Look for Plasmodium parasites.
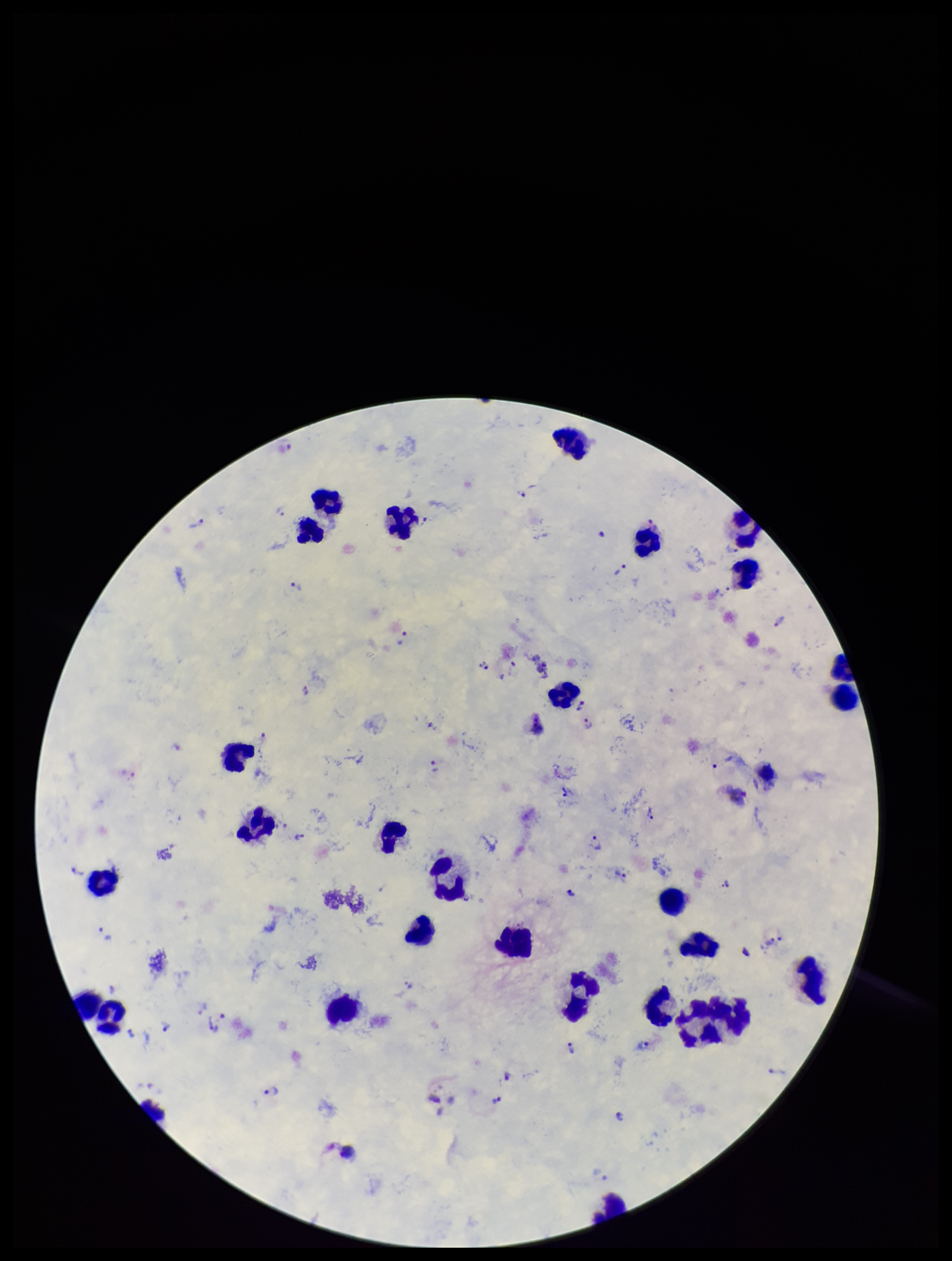
Detected.

Summary:
  - Patient malaria status: infected
  - Field of view: single
  - Preparation: thick blood smear
  - Image size: 952×1261 pixels
  - Capture: smartphone photograph through the microscope eyepiece
  - Species reported for this patient: Plasmodium vivax
  - Leukocyte count: 28
  - Parasite count: 46
  - Stain: Giemsa